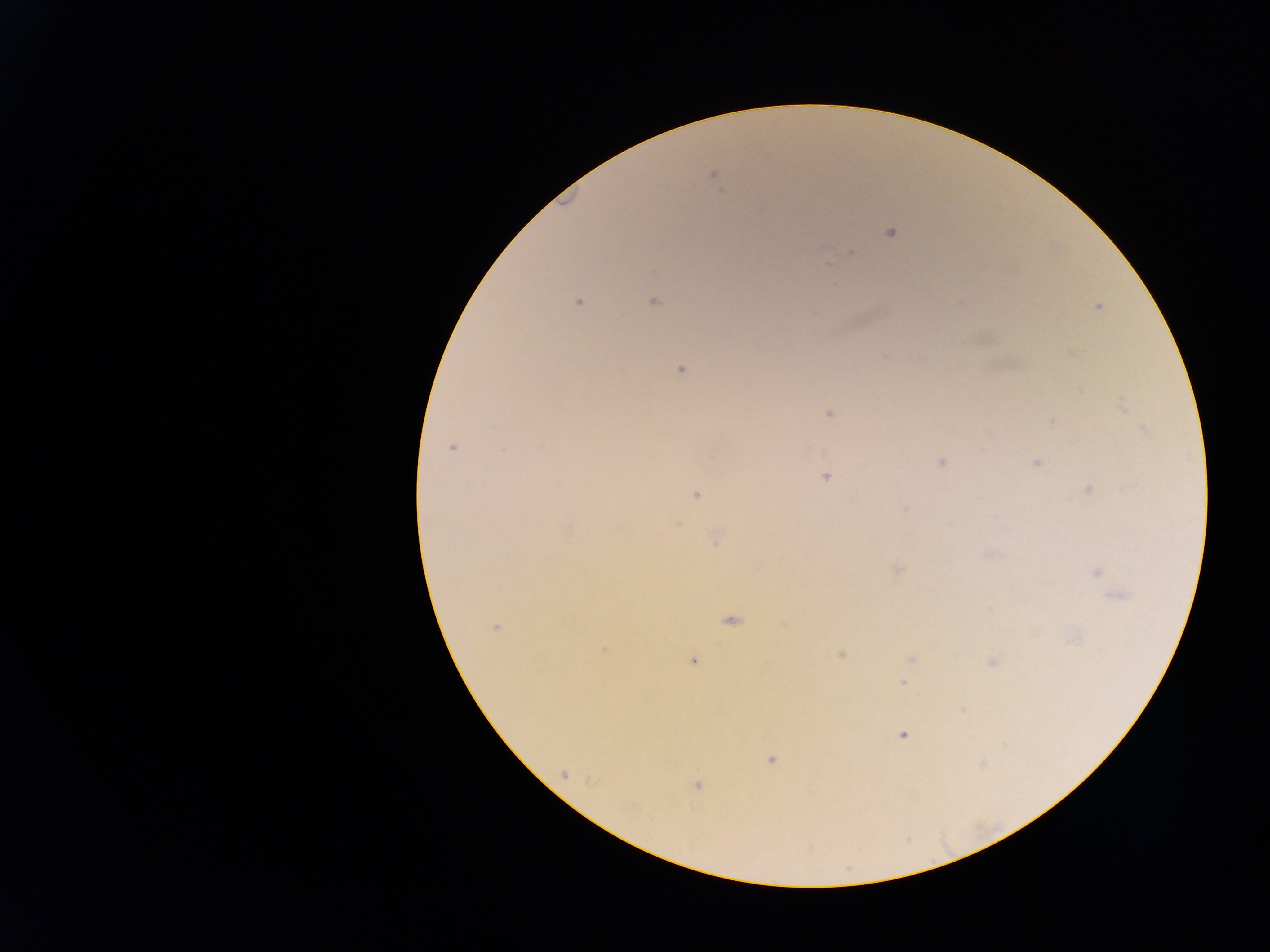

{
  "capture": "mobile-phone photograph through a microscope",
  "image_size": "1270×952 pixels",
  "preparation": "thick blood film",
  "field_of_view": "single",
  "country": "Ghana",
  "malaria_parasite_locations": "approximate centers as [x, y] in pixels: [713, 176], [890, 233], [850, 253], [578, 303], [653, 303], [1099, 307], [884, 357], [681, 370], [829, 414], [1051, 421], [451, 447], [941, 463], [1036, 463], [825, 477], [1089, 489], [696, 494], [905, 508], [678, 524], [567, 531], [717, 542], [898, 569], [1097, 572], [731, 620], [494, 628], [605, 650], [841, 655], [911, 658], [693, 661], [992, 662], [903, 683], [903, 735], [771, 759], [564, 774], [697, 786]"
}